Report the malaria status of this cell.
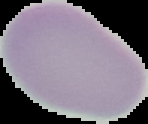
Uninfected.

Image is 148×124 pixels. Segmented cell region on a black background. From a thin blood film.